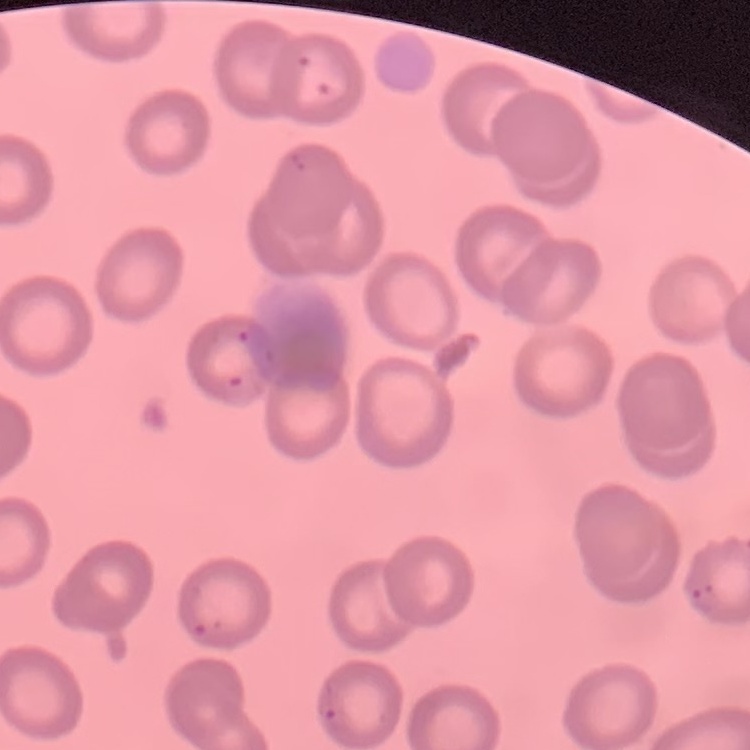

erythrocyte morphology = no rouleaux formation
stain = Field's or Giemsa
image type = square crop of a larger photomicrograph
preparation = thin peripheral smear